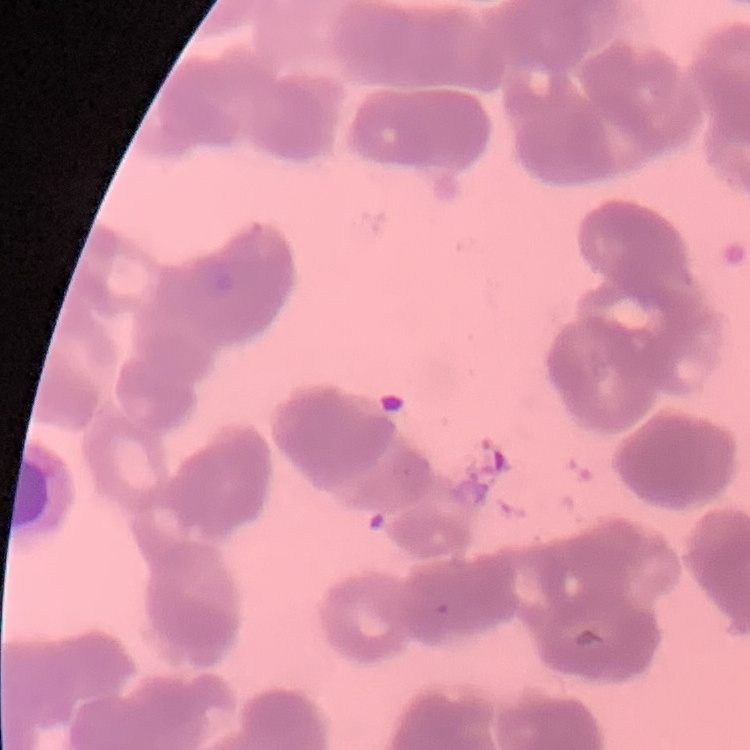

{
  "red_blood_cell_morphology": "rouleaux formation",
  "image_type": "one tile cut from a larger photomicrograph",
  "stain": "Field's or Giemsa",
  "preparation": "thin blood smear"
}